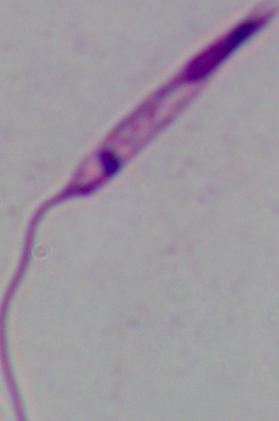

Micrograph. A Leishmania parasite is shown. Captured at 1000x magnification.